Identify the parasite.
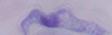
A trypanosome.

Photomicrograph. Captured at 1000x magnification.